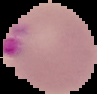 Result: malaria parasites detected. The area outside the segmented cell region is set to black. Image is 97×94 pixels. From a thin blood smear.